Identify the cell.
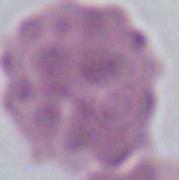

An erythrocyte.

Photomicrograph. 1000x magnification.